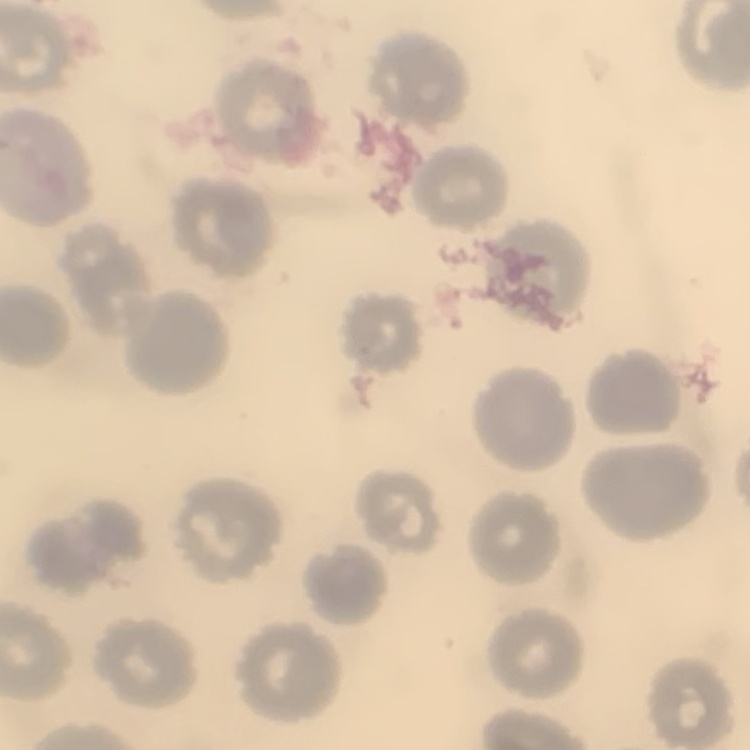

The red blood cells exhibit no rouleaux formation. Stained with either Field's or Giemsa. Thin blood film. Square crop of a larger photomicrograph.